Look for Plasmodium parasites.
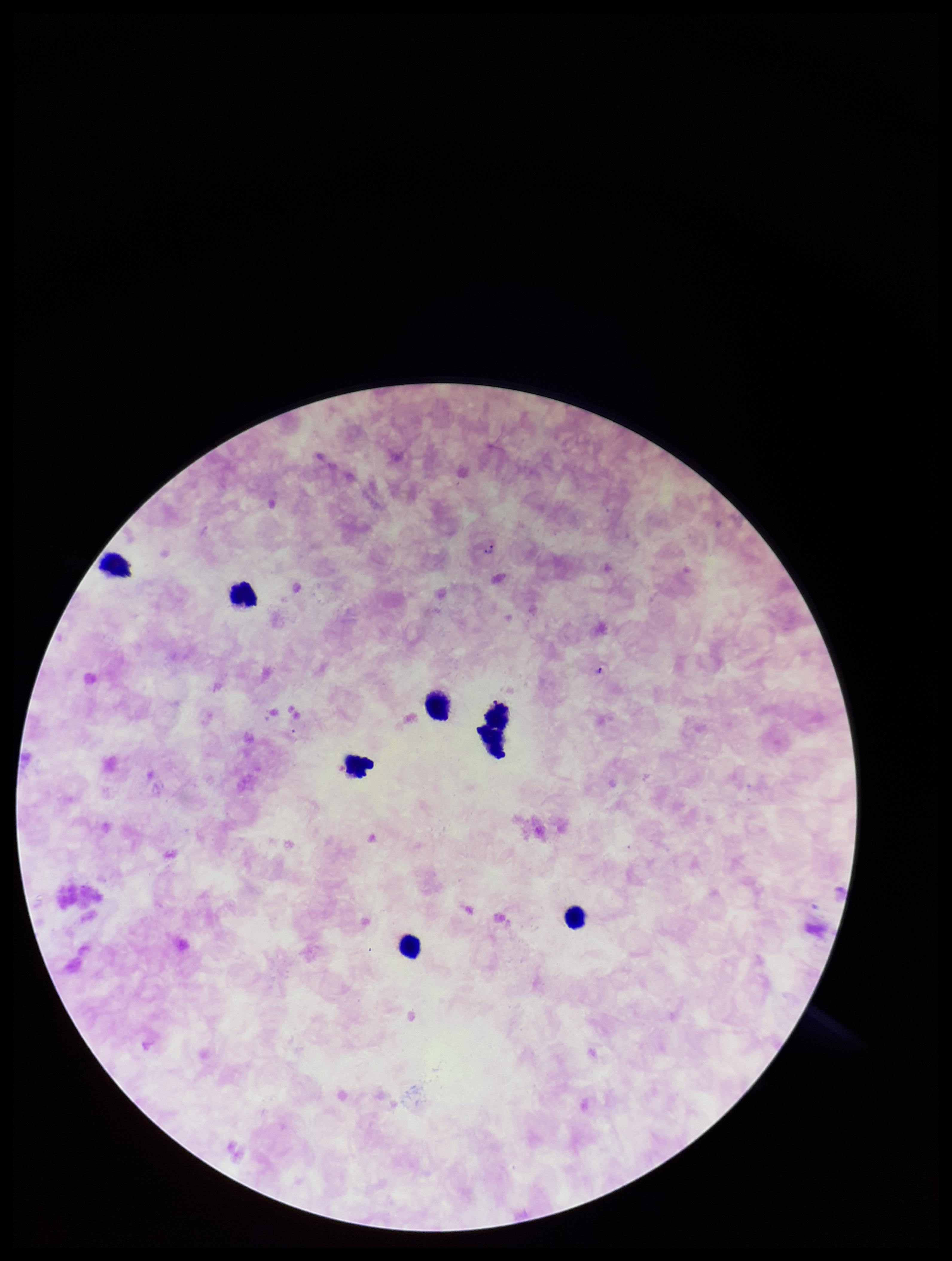

Seen.

Parasite count: 2. One field from this slide. Image is 952×1261 pixels. Species reported for this patient: Plasmodium falciparum. Smartphone photograph taken through the eyepiece of a microscope. Preparation: thick blood smear. Patient malaria status: positive. Stained with Giemsa. Leukocyte count: 7.